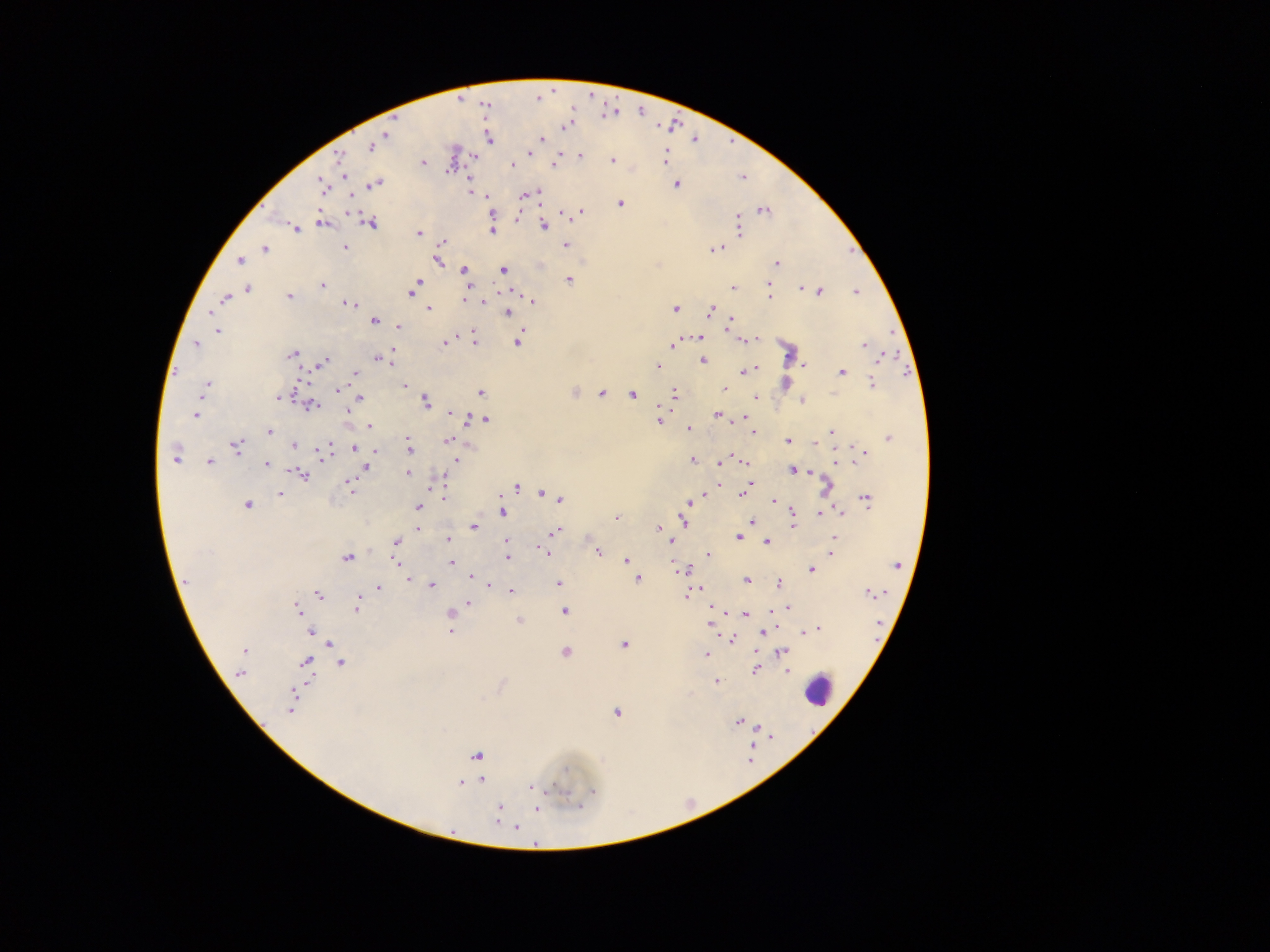

capture: mobile-phone photograph through a microscope
leukocyte_locations: 'approximate centers as {x, y} in pixels: {820, 692}'
malaria_parasite_locations: 'approximate centers as {x, y} in pixels: {565, 127}, {386, 134}, {489, 139}, {543, 139}, {371, 146}, {529, 153}, {580, 156}, {665, 157}, {340, 158}, {612, 160}, {423, 163}, {512, 164}, {553, 164}, {448, 170}, {344, 175}, {375, 184}, {322, 185}, {677, 185}, {471, 192}, {537, 194}, {487, 196}, {524, 196}, {621, 204}, {764, 211}, {581, 213}, {492, 216}, {322, 222}, {370, 224}, {543, 225}, {738, 225}, {295, 228}, {492, 230}, {418, 233}, {442, 242}, {566, 245}, {345, 247}, {264, 248}, {714, 249}, {239, 261}, {438, 261}, {777, 263}, {465, 270}, {504, 270}, {570, 279}, {418, 282}, {767, 284}, {321, 285}, {733, 287}, {248, 288}, {800, 288}, {769, 290}, {821, 291}, {856, 292}, {411, 293}, {288, 296}, {769, 296}, {225, 299}, {534, 301}, {481, 302}, {349, 304}, {429, 309}, {675, 309}, {711, 310}, {507, 313}, {374, 321}, {730, 323}, {399, 327}, {218, 331}, {700, 337}, {756, 339}, {474, 340}, {748, 340}, {518, 341}, {445, 343}, {197, 344}, {673, 345}, {864, 345}, {392, 352}, {789, 353}, {292, 354}, {883, 356}, {380, 359}, {388, 360}, {703, 361}, {323, 363}, {658, 365}, {805, 365}, {753, 369}, {746, 371}, {841, 372}, {355, 373}, {785, 383}, {872, 384}, {207, 385}, {404, 385}, {723, 388}, {338, 389}, {481, 392}, {602, 393}, {674, 393}, {631, 394}, {279, 397}, {756, 397}, {360, 399}, {802, 400}, {426, 401}, {311, 406}, {347, 410}, {452, 412}, {195, 415}, {718, 415}, {466, 417}, {744, 418}, {659, 419}, {486, 420}, {369, 426}, {689, 429}, {269, 431}, {752, 432}, {831, 432}, {888, 437}, {449, 440}, {787, 442}, {816, 443}, {293, 445}, {236, 446}, {409, 446}, {327, 448}, {355, 448}, {376, 450}, {864, 454}, {323, 457}, {176, 459}, {457, 460}, {692, 460}, {209, 461}, {744, 461}, {721, 462}, {839, 463}, {266, 464}, {365, 467}, {792, 470}, {408, 473}, {302, 476}, {347, 481}, {749, 484}, {350, 486}, {719, 486}, {827, 486}, {516, 488}, {280, 493}, {742, 493}, {544, 494}, {444, 497}, {700, 497}, {559, 499}, {867, 500}, {773, 501}, {688, 504}, {248, 505}, {418, 507}, {503, 512}, {685, 513}, {820, 513}, {826, 513}, {840, 513}, {793, 514}, {617, 517}, {683, 519}, {752, 522}, {792, 525}, {474, 527}, {659, 527}, {746, 527}, {418, 528}, {555, 531}, {738, 538}, {834, 538}, {447, 539}, {670, 540}, {395, 542}, {506, 542}, {767, 542}, {448, 543}, {545, 552}, {598, 552}, {831, 553}, {708, 554}, {507, 557}, {347, 558}, {626, 560}, {396, 562}, {451, 563}, {897, 565}, {679, 570}, {812, 570}, {470, 577}, {638, 579}, {187, 580}, {407, 580}, {746, 580}, {779, 582}, {488, 583}, {558, 583}, {432, 585}, {378, 588}, {698, 590}, {511, 591}, {869, 593}, {318, 594}, {687, 595}, {468, 603}, {357, 606}, {785, 607}, {297, 608}, {565, 611}, {450, 613}, {746, 615}, {519, 620}, {710, 623}, {815, 629}, {311, 632}, {450, 632}, {765, 632}, {806, 632}, {732, 640}, {624, 644}, {329, 645}, {244, 650}, {566, 652}, {784, 653}, {706, 654}, {305, 662}, {341, 663}, {755, 670}, {787, 671}, {240, 673}, {716, 681}, {292, 700}, {616, 713}, {738, 722}, {759, 727}, {476, 755}, {565, 770}, {482, 781}, {461, 783}, {531, 787}, {593, 792}, {499, 808}, {537, 809}, {498, 815}, {516, 827}'
country: Ghana
field_of_view: single
preparation: thick blood film
image_size: 1270×952 pixels